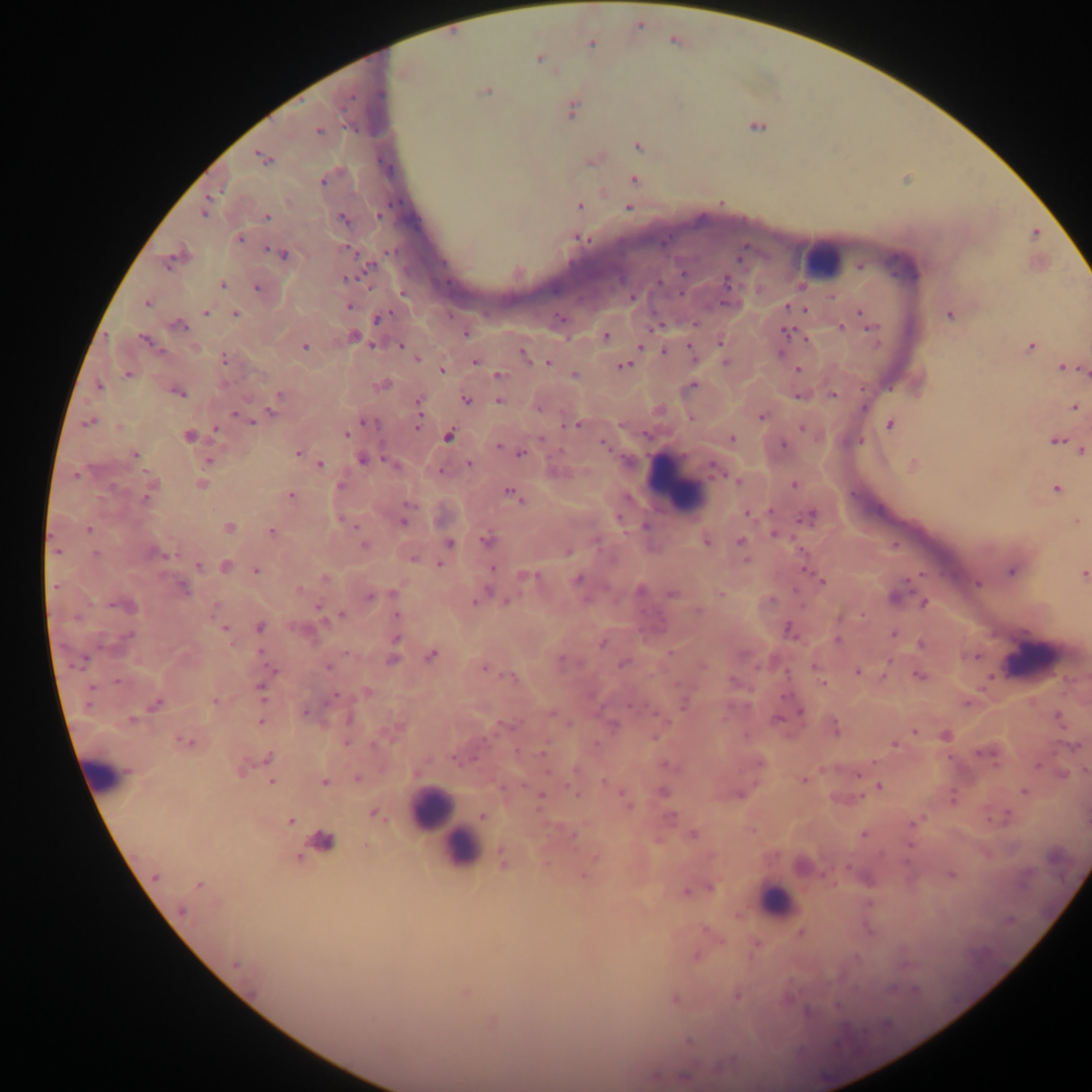
Approximate centers as x y in pixels.
Summary:
  - Leukocyte locations: 821 260; 674 485; 1033 660; 103 774; 431 808; 454 844; 776 902
  - Plasmodium parasite locations: 674 40; 591 43; 539 58; 486 90; 570 109; 756 125; 318 131; 638 145; 262 157; 594 158; 633 179; 579 205; 628 208; 204 209; 266 217; 342 219; 1034 233; 239 238; 580 238; 281 253; 175 256; 860 266; 345 277; 221 284; 257 287; 147 302; 349 305; 787 306; 804 308; 859 311; 205 312; 234 314; 950 314; 378 317; 179 326; 840 327; 870 328; 786 332; 465 333; 606 336; 353 337; 806 339; 145 340; 720 340; 372 344; 304 345; 401 345; 640 345; 1031 346; 664 351; 692 352; 524 354; 224 357; 416 358; 475 361; 725 361; 548 362; 623 365; 1063 367; 441 370; 798 370; 1083 370; 127 374; 499 375; 574 375; 382 385; 691 385; 99 386; 177 391; 833 394; 279 395; 799 395; 465 400; 499 401; 418 404; 274 406; 1073 406; 761 416; 691 417; 251 420; 89 422; 367 422; 417 424; 889 424; 577 425; 803 427; 216 428; 188 435; 345 435; 448 435; 730 438; 1055 439; 604 442; 498 445; 1081 450; 297 453; 521 453; 134 454; 362 459; 209 460; 395 464; 469 464; 319 465; 912 465; 715 469; 440 470; 737 480; 200 484; 794 484; 340 486; 1056 488; 150 489; 511 492; 290 495; 748 512; 809 516; 403 520; 1076 522; 228 528; 88 530; 271 531; 775 533; 487 539; 705 540; 448 542; 741 542; 363 545; 445 550; 568 551; 156 553; 411 556; 745 559; 440 563; 198 566; 225 567; 492 568; 256 570; 1012 570; 1083 574; 525 576; 324 577; 577 579; 822 580; 977 583; 181 587; 299 590; 639 590; 393 593; 721 593; 672 594; 370 595; 895 597; 476 600; 506 601; 924 602; 125 605; 319 608; 699 610; 340 615; 397 616; 259 627; 223 628; 787 628; 894 633; 396 639; 837 639; 922 644; 430 655; 392 659; 623 663; 328 666; 815 666; 484 668; 271 671; 857 672; 919 675; 511 677; 823 684; 261 688; 367 692; 333 697; 215 701; 683 703; 156 704; 305 712; 800 712; 551 713; 1058 718; 260 721; 613 725; 834 727; 914 730; 945 735; 184 741; 346 742; 895 744; 1076 746; 544 753; 987 753; 268 758; 455 758; 759 761; 666 766; 241 767; 1085 770; 858 773; 1062 773; 357 779; 802 779; 323 781; 271 782; 879 787; 662 791; 1024 792; 739 794; 540 796; 952 798; 626 799; 375 813; 482 815; 290 820; 912 822; 692 834; 863 834; 573 835; 320 842; 297 856; 594 857; 503 858; 802 865; 583 875; 950 875; 154 877; 198 884; 710 888; 686 890; 802 933; 696 956; 465 992; 737 995; 674 999; 491 1020; 689 1041
  - Capture: mobile-phone photograph through a microscope
  - Preparation: thick blood film
  - Country: Ghana
  - Field of view: single
  - Image size: 1092×1092 pixels